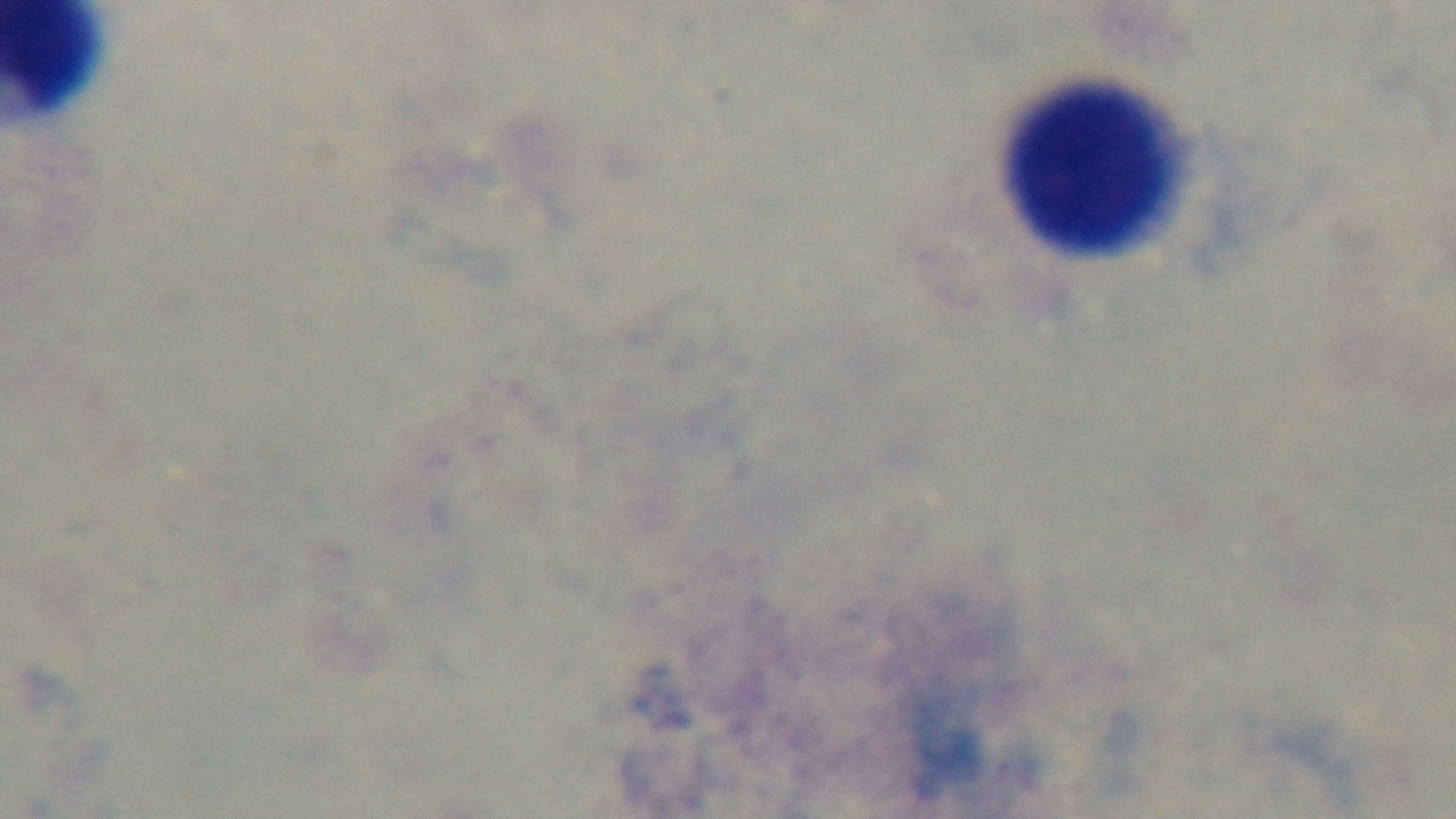 Malaria status: negative. 100x oil-immersion objective. One field from the slide. Giemsa-stained. Photomicrograph. Mounted 4K digital camera. Preparation: thick blood film.